Locate every leukocyte (white blood cell).
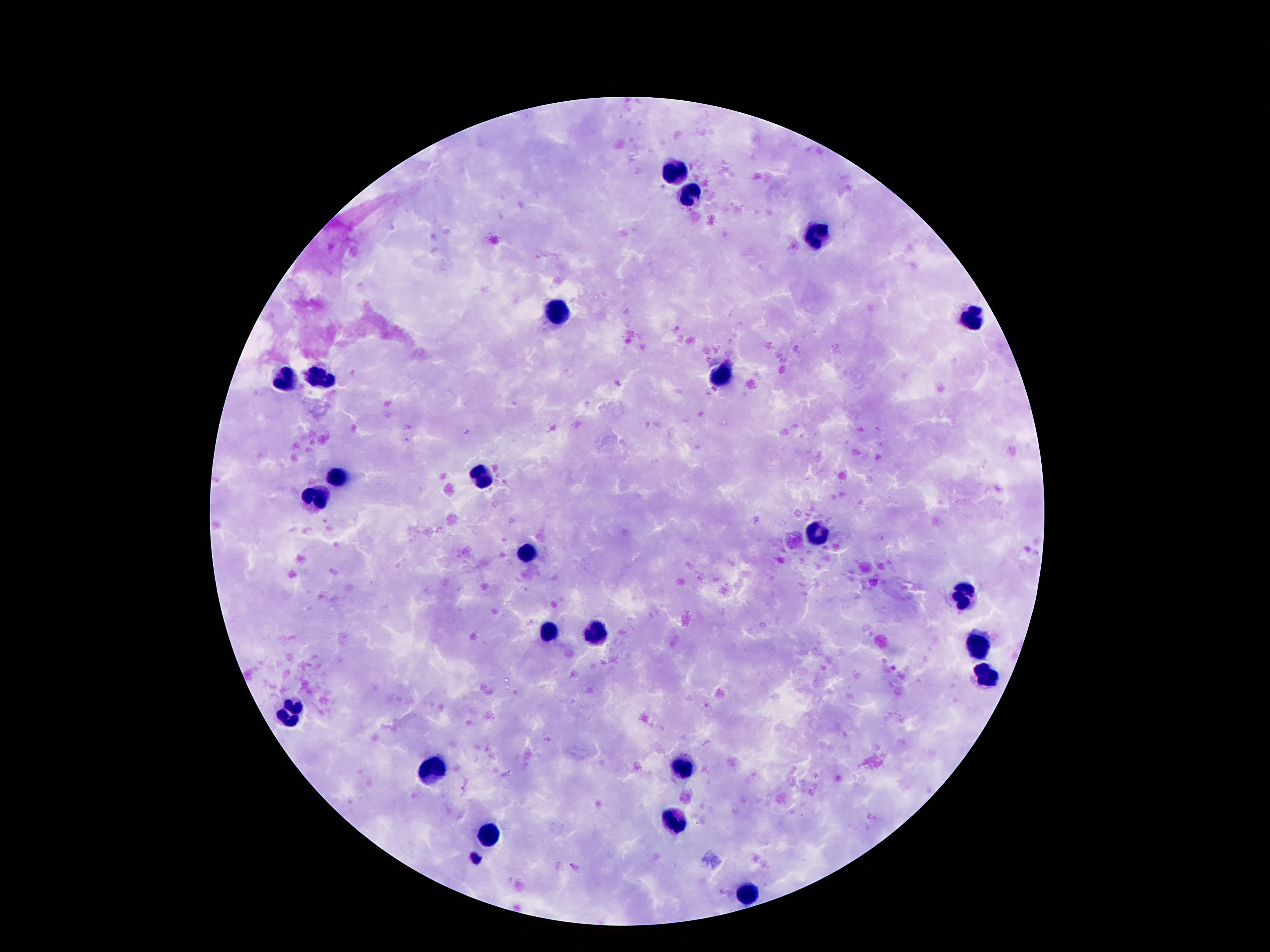

Approximate centers as {x, y} in pixels.
Leukocytes: {677, 175}, {694, 192}, {819, 238}, {560, 311}, {971, 318}, {281, 378}, {322, 378}, {722, 378}, {339, 476}, {481, 478}, {318, 495}, {820, 536}, {526, 551}, {964, 595}, {549, 631}, {598, 635}, {976, 647}, {985, 678}, {292, 707}, {686, 767}, {434, 769}, {673, 818}, {488, 839}, {747, 895}.

100x magnification. Photographed through the microscope eyepiece with a smartphone camera. Image is 1270×952 pixels. One field from this slide. Thick peripheral-blood smear. Giemsa stain. Patient malaria status: uninfected.